State which parasite is depicted.
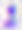

This is Toxoplasma gondii.

Micrograph. Captured at 400x magnification.